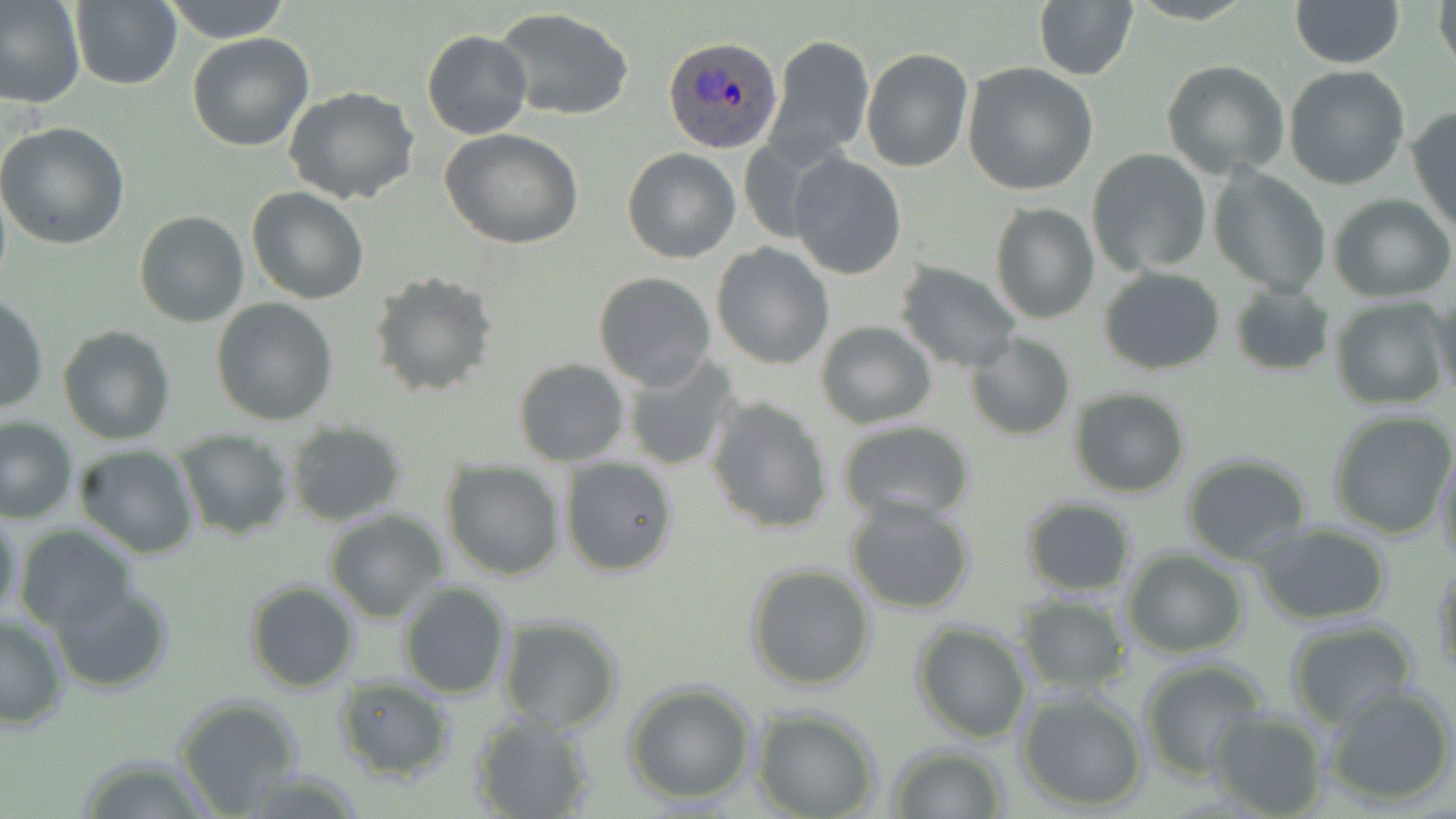
Summary:
  - Coordinate format: approximate bounding boxes as [x1, y1, x2, y2] in pixels
  - Plasmodium ovale-infected red blood cell locations: [663, 37, 784, 154]
  - Uninfected red blood cell locations: [160, 0, 294, 44], [1032, 0, 1139, 83], [1288, 0, 1405, 68], [1432, 0, 1455, 79], [0, 1, 86, 108], [68, 1, 183, 89], [495, 7, 635, 122], [422, 31, 531, 140], [186, 32, 314, 151], [766, 34, 874, 166], [861, 48, 973, 172], [1161, 60, 1291, 180], [962, 62, 1098, 195], [1283, 65, 1411, 191], [284, 88, 421, 205], [1409, 106, 1456, 234], [0, 121, 132, 250], [440, 127, 584, 249], [622, 147, 741, 263], [1086, 150, 1213, 277], [789, 152, 905, 278], [1208, 165, 1332, 298], [246, 186, 369, 306], [1330, 195, 1455, 302], [988, 200, 1101, 325], [134, 211, 250, 328], [711, 243, 834, 371], [893, 261, 1023, 371], [1098, 266, 1226, 375], [367, 269, 497, 397], [593, 272, 717, 392], [1228, 283, 1335, 377], [1429, 292, 1456, 405], [1, 295, 48, 417], [211, 296, 341, 426], [1330, 296, 1451, 408], [814, 320, 938, 430], [58, 325, 176, 444], [964, 334, 1076, 441], [622, 356, 744, 473], [512, 358, 629, 467], [1067, 388, 1190, 497], [704, 396, 834, 535], [1324, 408, 1456, 539], [0, 417, 77, 524], [283, 421, 408, 528], [835, 421, 976, 526], [173, 428, 296, 540], [72, 444, 200, 560], [1434, 444, 1456, 573], [1181, 452, 1315, 565], [557, 455, 681, 578], [439, 461, 566, 582], [845, 494, 976, 615], [1019, 497, 1137, 597], [0, 505, 24, 632], [322, 509, 451, 622], [1252, 524, 1394, 624], [13, 525, 138, 633], [1121, 549, 1248, 658], [745, 562, 879, 691], [1432, 562, 1455, 682], [244, 578, 361, 692], [396, 581, 512, 699], [50, 584, 175, 694], [1013, 594, 1131, 697], [0, 613, 71, 731], [495, 615, 624, 734], [1282, 620, 1423, 731], [911, 621, 1032, 744], [1136, 657, 1270, 780], [330, 679, 456, 783], [623, 681, 758, 806], [1321, 682, 1454, 807], [1014, 688, 1149, 812], [174, 695, 304, 812], [751, 707, 881, 819], [1204, 707, 1331, 819], [468, 712, 598, 819], [883, 743, 1010, 818], [73, 753, 216, 817]
  - Slide-level diagnosis: Plasmodium ovale
  - Image size: 1456×819 pixels
  - Field of view: single
  - Preparation: thin blood film
  - Modality: light microscopy
  - Stain: May-Grünwald-Giemsa
  - Magnification: 1000x